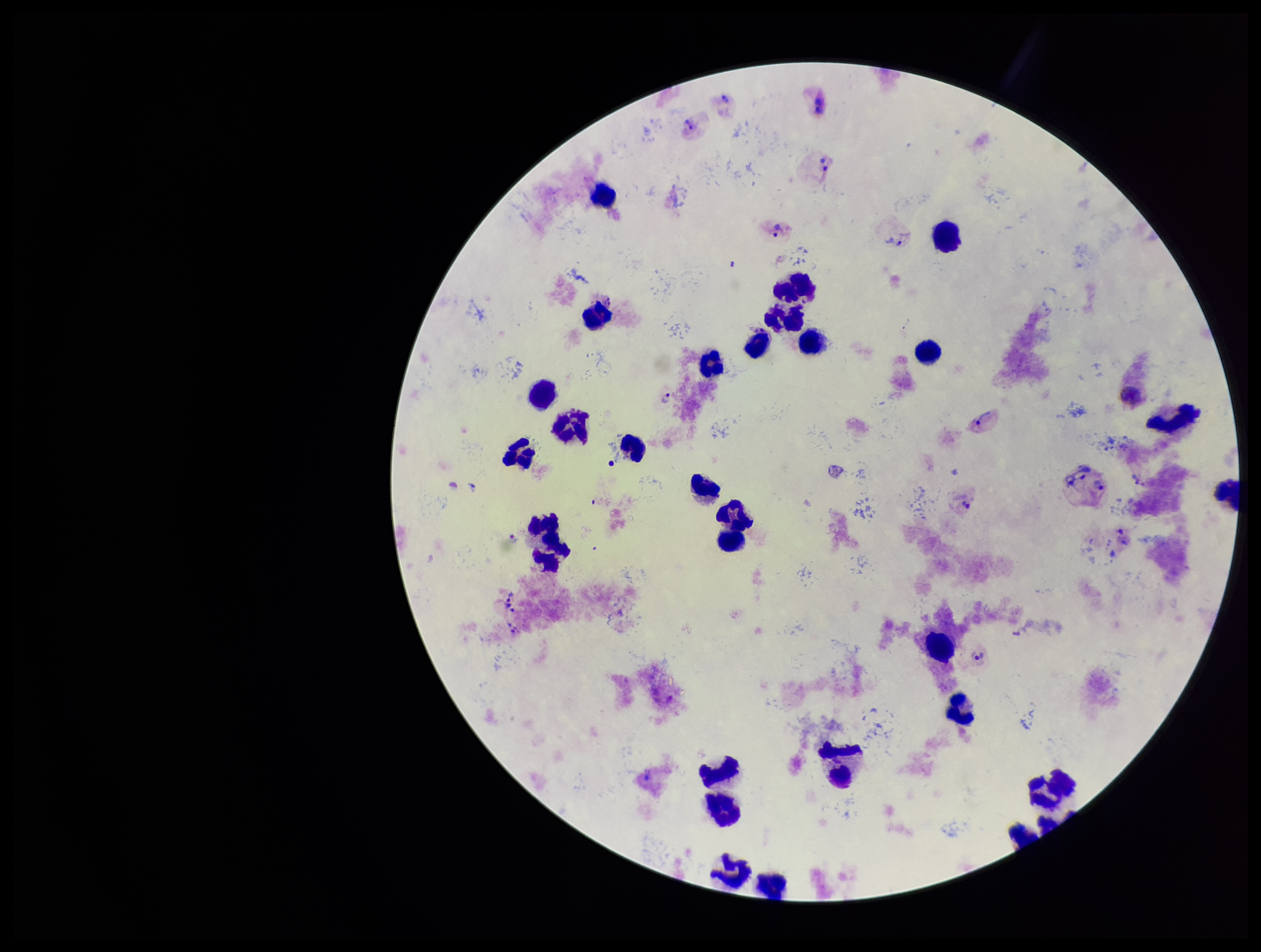

Summary:
  - Patient malaria status: infected
  - Plasmodium parasites: seen
  - Stain: Giemsa
  - Preparation: thick
  - Parasite count: 12
  - Species reported for this patient: Plasmodium vivax
  - Field of view: one from this slide
  - Leukocyte count: 30
  - Capture: smartphone photograph through the microscope eyepiece
  - Image size: 1261×952 pixels